Give the position of every leukocyte visible.
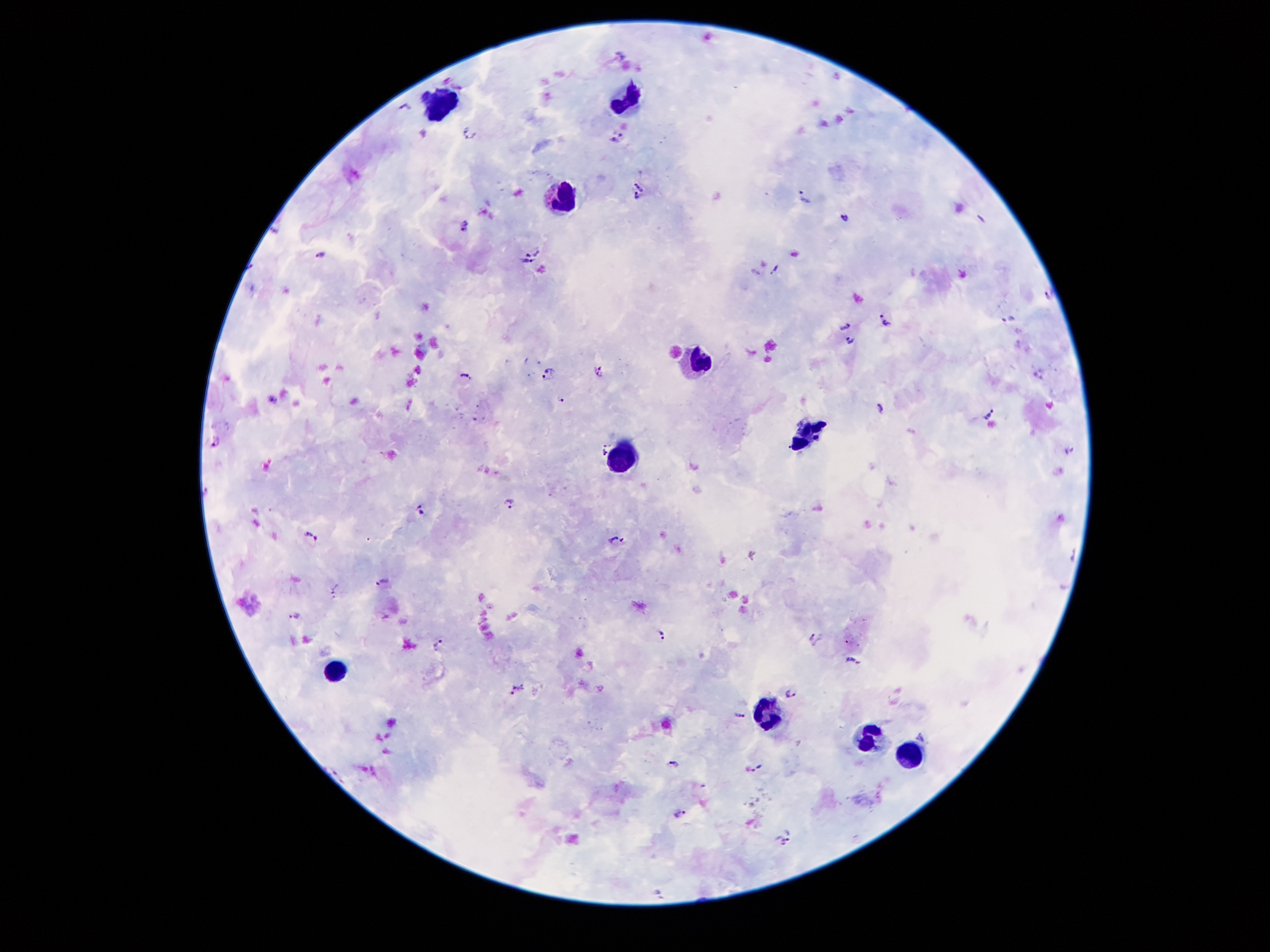
Approximate centers as (x, y) in pixels.
Leukocytes: (625, 96), (447, 99), (565, 200), (696, 358), (808, 434), (623, 455), (339, 672), (770, 722), (869, 730), (909, 750).

Plasmodium parasite locations = (408, 106), (619, 136), (472, 138), (641, 184), (804, 198), (634, 199), (845, 220), (465, 227), (532, 247), (321, 253), (527, 265), (775, 270), (1050, 293), (1009, 319), (886, 321), (846, 326), (849, 341), (598, 368), (548, 372), (1039, 372), (465, 376), (560, 397), (880, 406), (991, 411), (217, 440), (604, 446), (1068, 450), (511, 503), (421, 510), (312, 533), (616, 542), (1070, 556), (381, 583), (296, 616), (663, 633), (814, 638), (438, 643), (854, 661), (517, 690), (789, 693), (740, 715), (921, 737), (673, 765), (758, 766), (679, 814), (790, 831), (777, 847), (658, 893)
magnification = 100x
preparation = thick peripheral-blood smear
field of view = single
image size = 1270×952 pixels
capture = smartphone camera through the microscope eyepiece
patient malaria status = infected with Plasmodium falciparum
stain = Giemsa